Assess the morphology of the erythrocytes.
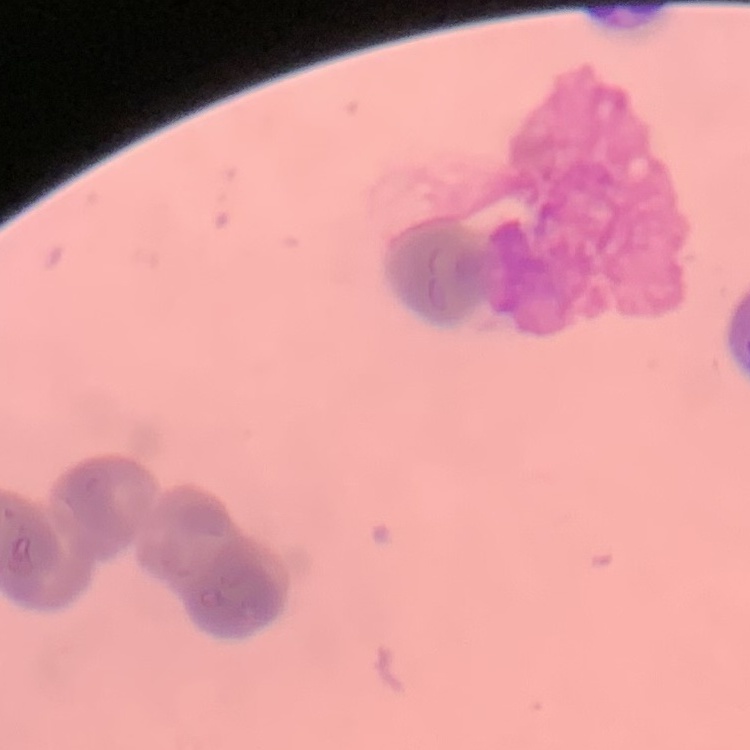

They show rouleaux formation.

Thin blood smear. Square crop of a larger photomicrograph. Stained with either Field's or Giemsa.